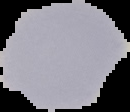
Summary:
  - Malaria status: uninfected
  - Image size: 130×112 pixels
  - Preparation: thin blood smear
  - Image type: segmented cell region with the area outside set to black